Assess this cell for malaria.
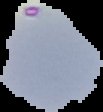
Uninfected.

Summary:
  - Image size: 103×112 pixels
  - Preparation: thin blood film
  - Image type: segmented cell region with the area outside set to black